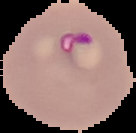
Malaria status: parasitized. Cell region segmented out of the field of view; the surrounding area is masked to black. From a thin blood smear. Image is 136×133 pixels.